Locate and identify every blood parasite.
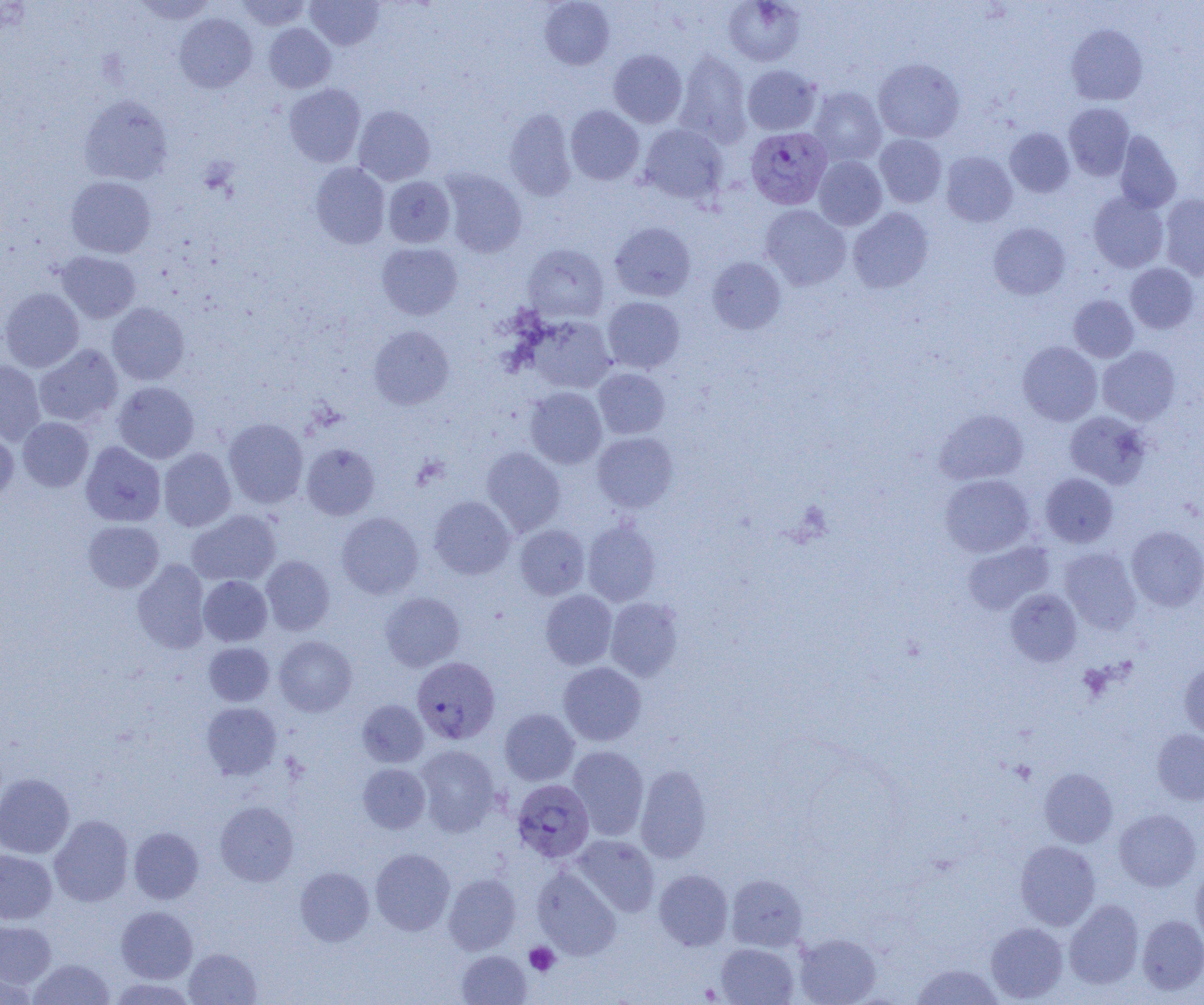
Approximate bounding boxes as (x1,y1)-(x2,y2) corner pairs in pixels.
Plasmodium vivax-infected red blood cells: (745,127)-(832,209), (412,656)-(500,744), (512,779)-(594,863).
No Plasmodium falciparum, Plasmodium ovale, Plasmodium malariae, Babesia divergens, or Trypanosoma brucei observed.

Summary:
  - Uninfected red blood cell locations: (131,0)-(217,24), (236,0)-(311,30), (305,0)-(384,50), (539,0)-(615,70), (723,0)-(806,66), (175,13)-(257,92), (264,23)-(336,93), (1066,23)-(1148,105), (608,49)-(688,128), (675,50)-(753,148), (873,58)-(965,143), (742,64)-(822,135), (284,84)-(365,167), (808,87)-(886,166), (78,95)-(174,185), (1064,103)-(1134,180), (353,105)-(435,185), (566,106)-(644,185), (503,109)-(576,200), (639,124)-(728,205), (1005,127)-(1074,197), (1114,131)-(1182,213), (874,134)-(947,207), (940,151)-(1017,227), (813,156)-(887,230), (310,162)-(390,249), (441,169)-(527,258), (66,176)-(156,258), (383,176)-(455,247), (1088,191)-(1169,272), (1159,194)-(1204,280), (760,204)-(851,290), (847,207)-(933,293), (609,222)-(696,301), (988,223)-(1071,299), (377,242)-(462,320), (523,243)-(608,322), (56,251)-(141,323), (707,257)-(786,334), (1125,263)-(1198,333), (0,287)-(84,372), (1068,295)-(1138,362), (602,297)-(684,373), (107,302)-(189,385), (527,315)-(616,393), (369,325)-(454,409), (1017,341)-(1102,425), (34,344)-(123,427), (1097,346)-(1180,425), (0,359)-(46,445), (593,368)-(670,439), (113,381)-(199,463), (525,387)-(607,468), (934,409)-(1028,484), (1064,411)-(1151,489), (18,417)-(93,492), (223,417)-(308,508), (0,427)-(19,506), (592,432)-(678,512), (81,441)-(166,527), (301,443)-(379,520), (481,447)-(565,535), (159,448)-(236,531), (1041,472)-(1118,547), (940,474)-(1034,557), (428,496)-(515,579), (186,509)-(281,586), (336,512)-(424,599), (582,519)-(661,606), (83,520)-(164,593), (514,524)-(590,600), (1126,525)-(1204,611), (963,540)-(1054,615), (1059,548)-(1141,633), (261,555)-(335,635), (132,560)-(210,653), (198,575)-(272,646), (1005,589)-(1081,666), (540,590)-(617,669), (380,592)-(465,671), (605,597)-(683,681), (274,636)-(357,716), (204,642)-(274,706), (1179,660)-(1204,740), (558,661)-(646,746), (357,699)-(428,767), (201,702)-(282,779), (500,708)-(579,785), (1151,728)-(1204,805), (414,744)-(500,835), (567,745)-(649,840), (358,763)-(430,834), (635,764)-(712,863), (1039,768)-(1117,847), (0,773)-(75,858), (215,801)-(298,886), (1114,808)-(1201,892), (49,815)-(133,907), (129,827)-(203,903), (572,834)-(660,917), (1015,840)-(1100,930), (370,848)-(455,935), (0,849)-(57,924), (1191,864)-(1204,949), (295,866)-(374,946), (531,866)-(621,959), (654,869)-(733,951), (443,872)-(521,955), (726,874)-(807,951), (1064,899)-(1144,989), (116,906)-(198,983), (1137,915)-(1204,995), (0,920)-(57,988), (985,922)-(1068,1003), (794,932)-(881,1005), (715,942)-(798,1004), (184,948)-(261,1005), (457,950)-(531,1005), (29,958)-(115,1004), (911,963)-(1003,1005), (0,966)-(37,1004), (108,977)-(197,1005)
  - Platelet locations: (1010,760)-(1037,784), (524,942)-(560,976)
  - Slide-level diagnosis: Plasmodium vivax
  - Image size: 1204×1005 pixels
  - Modality: optical microscopy
  - Field of view: single
  - Magnification: 1000x
  - Preparation: thin blood smear